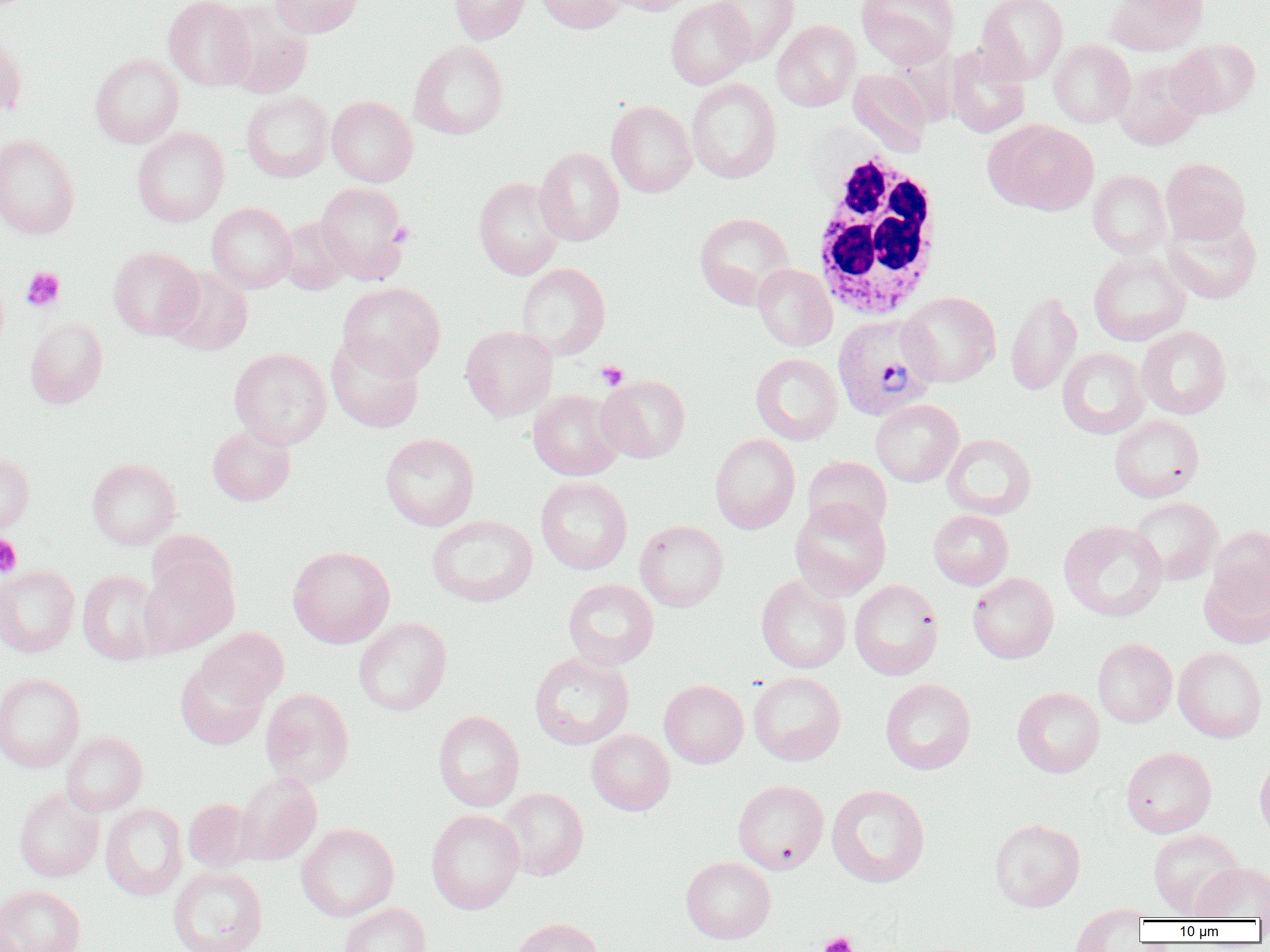
Approximate bounding boxes as (x1, y1, x2, y2) in pixels. Plasmodium vivax-infected red blood cell locations: (832, 313, 938, 421). Platelet locations: (389, 222, 415, 247), (21, 267, 65, 312), (596, 361, 629, 390), (0, 533, 22, 578), (819, 932, 857, 952). White blood cell locations: (808, 150, 944, 320). Uninfected red blood cell locations: (163, 0, 255, 90), (269, 0, 366, 38), (448, 0, 531, 44), (536, 0, 625, 34), (605, 0, 698, 15), (856, 0, 959, 68), (975, 0, 1068, 84), (1104, 0, 1208, 55), (665, 1, 754, 89), (708, 1, 799, 63), (221, 2, 313, 98), (772, 20, 860, 111), (0, 29, 27, 121), (1169, 38, 1260, 118), (1049, 39, 1135, 128), (408, 40, 509, 140), (945, 45, 1030, 138), (90, 54, 183, 148), (1114, 58, 1205, 151), (848, 69, 932, 156), (686, 78, 781, 184), (241, 91, 333, 182), (327, 96, 417, 187), (606, 100, 696, 197), (985, 120, 1099, 215), (132, 127, 229, 227), (0, 134, 80, 239), (534, 146, 624, 246), (1161, 158, 1250, 244), (1088, 169, 1171, 258), (473, 177, 565, 280), (315, 182, 411, 285), (206, 202, 296, 293), (694, 212, 794, 309), (1162, 213, 1262, 304), (277, 217, 352, 294), (108, 246, 203, 340), (1088, 250, 1190, 346), (516, 262, 611, 360), (752, 263, 837, 351), (162, 267, 253, 355), (338, 282, 445, 379), (1005, 290, 1082, 396), (899, 291, 1000, 387), (25, 318, 108, 408), (461, 326, 558, 421), (1136, 326, 1232, 419), (326, 335, 424, 433), (1057, 347, 1150, 439), (229, 348, 331, 449), (751, 353, 843, 445), (596, 374, 691, 462), (528, 389, 625, 481), (870, 400, 963, 487), (1109, 414, 1204, 502), (207, 424, 295, 505), (380, 433, 479, 531), (942, 433, 1036, 519), (710, 434, 800, 534), (0, 453, 34, 535), (803, 456, 892, 536), (87, 458, 181, 549), (535, 477, 632, 574), (1128, 497, 1223, 586), (790, 498, 891, 600), (928, 510, 1013, 590), (426, 515, 538, 606), (635, 520, 728, 612), (1059, 520, 1167, 621), (1208, 526, 1270, 612), (288, 545, 394, 648), (139, 554, 238, 657), (1199, 564, 1270, 649), (0, 565, 80, 657), (78, 570, 165, 665), (968, 573, 1059, 663), (756, 575, 851, 673), (563, 579, 659, 670), (849, 579, 944, 680), (353, 617, 452, 716), (198, 627, 289, 707), (1092, 638, 1177, 728), (1173, 647, 1267, 743), (528, 652, 634, 749), (175, 658, 269, 750), (749, 672, 846, 766), (0, 673, 85, 773), (880, 678, 976, 775), (659, 680, 748, 768), (1012, 687, 1104, 777), (260, 688, 354, 789), (433, 710, 524, 811), (586, 729, 675, 815), (61, 732, 147, 816), (1121, 747, 1216, 837), (1255, 754, 1270, 846), (234, 772, 321, 865), (732, 780, 829, 874), (826, 784, 930, 887), (13, 786, 104, 882), (498, 787, 588, 880), (14, 798, 187, 889), (183, 799, 256, 872), (100, 803, 187, 901), (426, 809, 524, 914), (989, 819, 1085, 911), (296, 823, 399, 921), (1148, 828, 1244, 919), (681, 857, 775, 943), (1190, 861, 1270, 921), (167, 865, 268, 952), (0, 885, 85, 952), (339, 903, 431, 952), (1070, 905, 1147, 951), (510, 918, 603, 952). Slide-level diagnosis: Plasmodium vivax. Captured at 1000x magnification. Single field of view. Image is 1270×952 pixels. Light microscopy. Thin blood smear.